Classify this cell by malaria status.
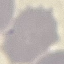

It is uninfected.

Thin blood smear. Cell patch, automatically extracted from a larger field of view and resized to 64 × 64 pixels. Giemsa stain. Acquired by smartphone through the microscope eyepiece.